Give the preparation type.
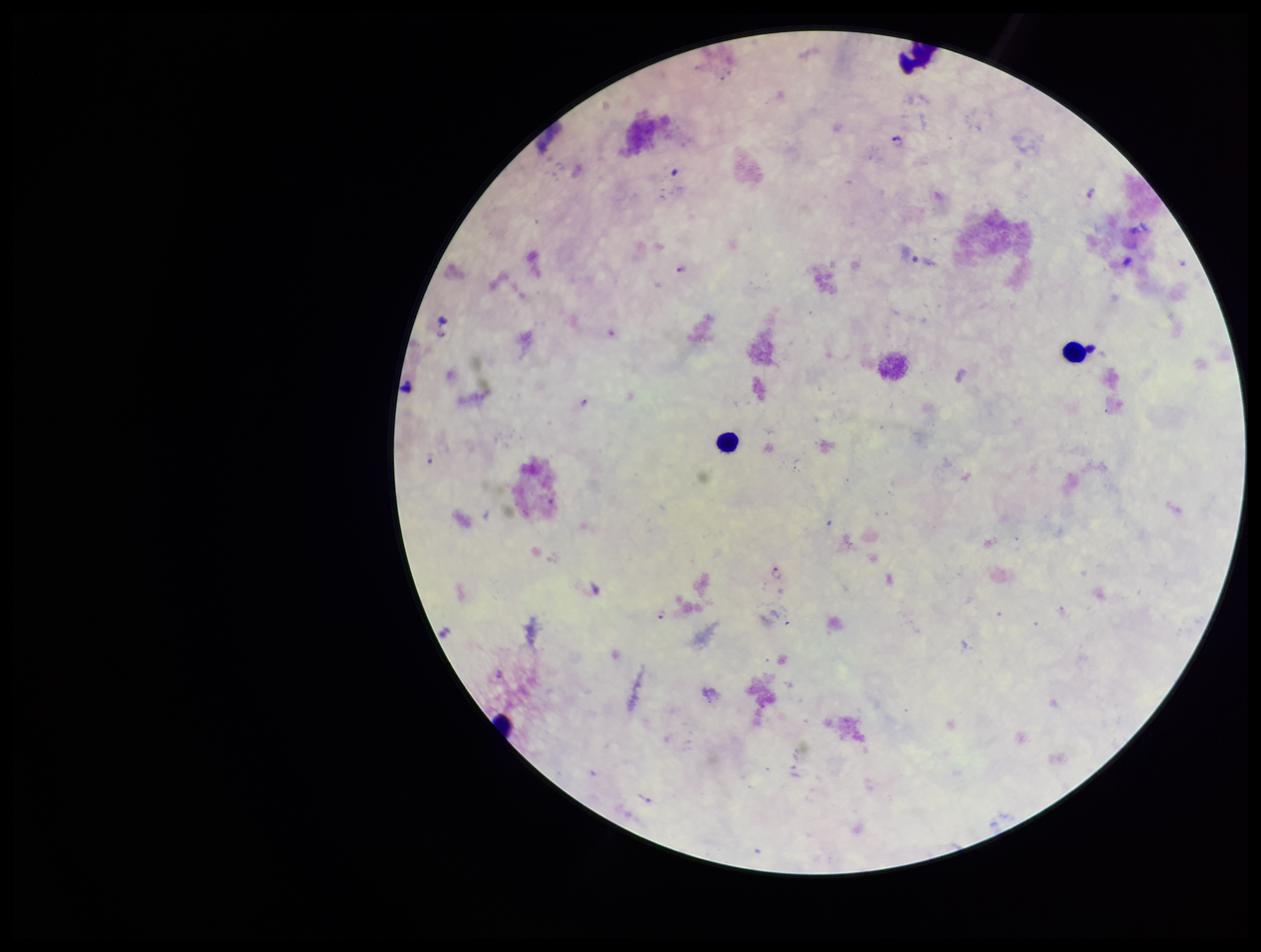
Thick.

Parasite count: 5. Photographed through the microscope eyepiece with a smartphone camera. Single field of view. Species reported for this patient: Plasmodium falciparum. Patient malaria status: positive. Giemsa stain. Plasmodium parasites: identified. Leukocyte count: 3. Image is 1261×952 pixels.